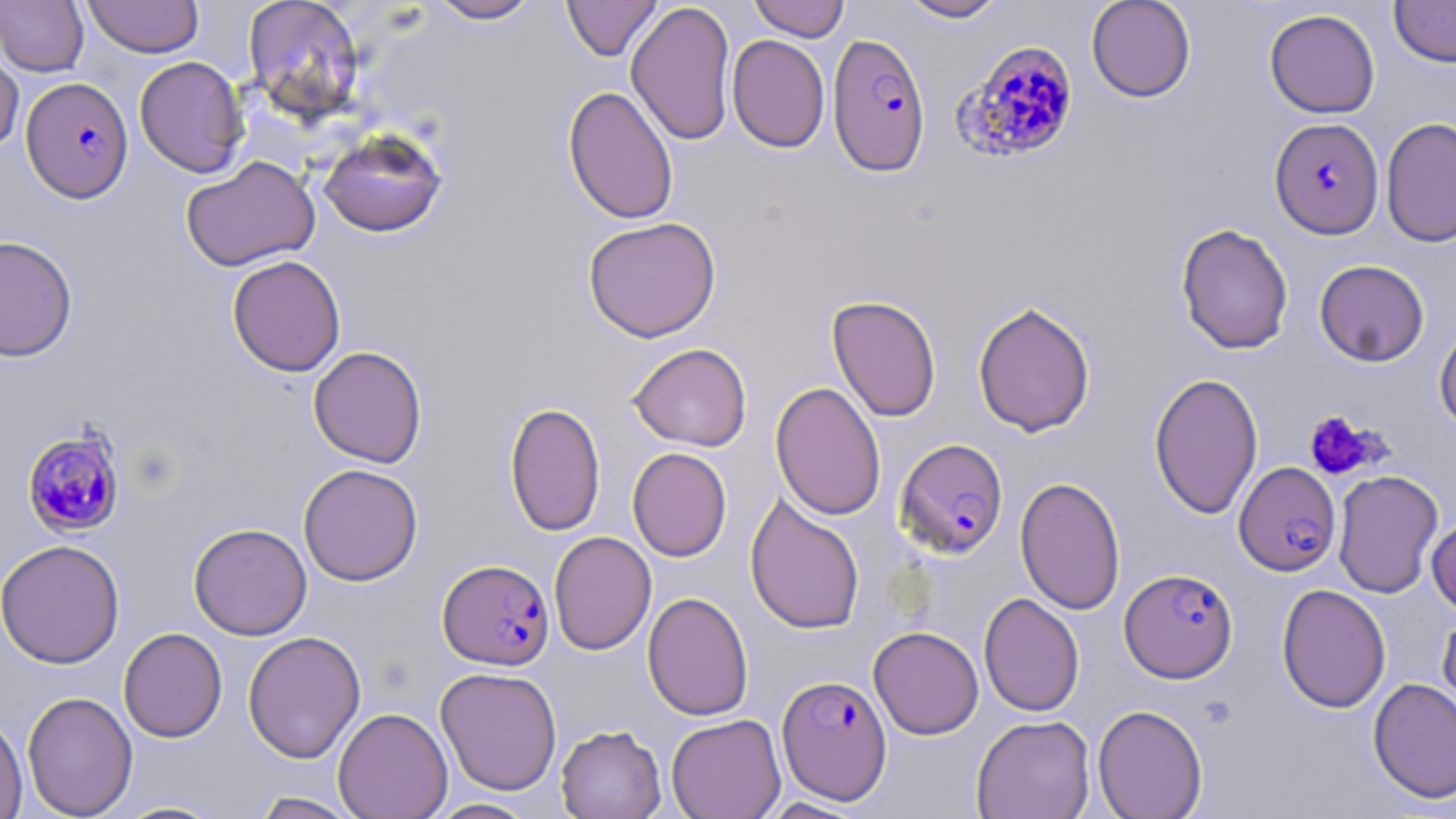
slide-level diagnosis = Plasmodium falciparum
stain = May-Grünwald-Giemsa
field of view = single
uninfected red blood cell locations = approximate bounding boxes as named x1/y1/x2/y2 corners in pixels: (x1=0, y1=0, x2=89, y2=76), (x1=83, y1=0, x2=203, y2=58), (x1=242, y1=0, x2=366, y2=122), (x1=426, y1=0, x2=542, y2=24), (x1=561, y1=0, x2=663, y2=62), (x1=748, y1=0, x2=850, y2=41), (x1=897, y1=0, x2=1009, y2=23), (x1=1086, y1=0, x2=1196, y2=103), (x1=1389, y1=0, x2=1456, y2=67), (x1=626, y1=1, x2=737, y2=146), (x1=1264, y1=8, x2=1380, y2=118), (x1=727, y1=34, x2=829, y2=153), (x1=0, y1=42, x2=25, y2=156), (x1=133, y1=56, x2=249, y2=178), (x1=563, y1=85, x2=679, y2=225), (x1=1381, y1=117, x2=1456, y2=248), (x1=318, y1=128, x2=448, y2=238), (x1=180, y1=156, x2=320, y2=272), (x1=582, y1=216, x2=722, y2=342), (x1=1175, y1=222, x2=1293, y2=355), (x1=0, y1=234, x2=79, y2=362), (x1=227, y1=255, x2=347, y2=377), (x1=1313, y1=259, x2=1430, y2=366), (x1=826, y1=294, x2=942, y2=422), (x1=972, y1=300, x2=1096, y2=437), (x1=1433, y1=319, x2=1456, y2=434), (x1=628, y1=343, x2=752, y2=452), (x1=308, y1=346, x2=428, y2=467), (x1=1148, y1=372, x2=1263, y2=520), (x1=770, y1=381, x2=886, y2=521), (x1=505, y1=401, x2=606, y2=536), (x1=627, y1=447, x2=731, y2=562), (x1=298, y1=463, x2=423, y2=586), (x1=1332, y1=470, x2=1444, y2=599), (x1=1015, y1=476, x2=1126, y2=615), (x1=744, y1=492, x2=866, y2=635), (x1=1426, y1=514, x2=1456, y2=616), (x1=188, y1=523, x2=312, y2=641), (x1=548, y1=531, x2=656, y2=655), (x1=0, y1=538, x2=125, y2=669), (x1=1276, y1=583, x2=1391, y2=713), (x1=642, y1=591, x2=754, y2=721), (x1=979, y1=592, x2=1084, y2=717), (x1=1437, y1=609, x2=1456, y2=732), (x1=868, y1=626, x2=984, y2=739), (x1=118, y1=627, x2=227, y2=742), (x1=243, y1=631, x2=366, y2=763), (x1=435, y1=666, x2=562, y2=796), (x1=1368, y1=677, x2=1456, y2=804), (x1=22, y1=690, x2=138, y2=818), (x1=1092, y1=704, x2=1208, y2=819), (x1=333, y1=707, x2=453, y2=819), (x1=0, y1=711, x2=28, y2=819), (x1=665, y1=714, x2=786, y2=819), (x1=971, y1=714, x2=1095, y2=819), (x1=555, y1=724, x2=667, y2=819), (x1=249, y1=791, x2=363, y2=818), (x1=757, y1=796, x2=871, y2=818), (x1=427, y1=798, x2=538, y2=818), (x1=114, y1=800, x2=227, y2=818)
image size = 1456×819 pixels
magnification = 1000x
preparation = thin blood smear
Plasmodium falciparum-infected red blood cell locations = approximate bounding boxes as named x1/y1/x2/y2 corners in pixels: (x1=827, y1=32, x2=931, y2=177), (x1=954, y1=40, x2=1081, y2=163), (x1=20, y1=76, x2=133, y2=202), (x1=1268, y1=118, x2=1384, y2=240), (x1=21, y1=427, x2=127, y2=538), (x1=895, y1=438, x2=1008, y2=558), (x1=1234, y1=461, x2=1341, y2=576), (x1=438, y1=559, x2=555, y2=670), (x1=1119, y1=568, x2=1238, y2=683), (x1=776, y1=674, x2=893, y2=804)
platelet locations = approximate bounding boxes as named x1/y1/x2/y2 corners in pixels: (x1=1302, y1=409, x2=1384, y2=480)
modality = light microscopy